Report the malaria status of this cell.
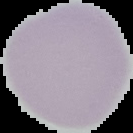

It is uninfected.

Summary:
  - Preparation: thin blood smear
  - Image type: segmented cell region with the area outside set to black
  - Image size: 133×133 pixels